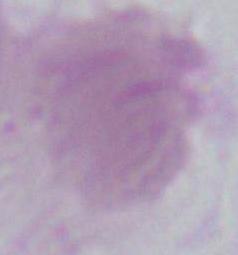
magnification: 1000x
modality: micrograph
identification: erythrocyte